Assess the morphology of the erythrocytes.
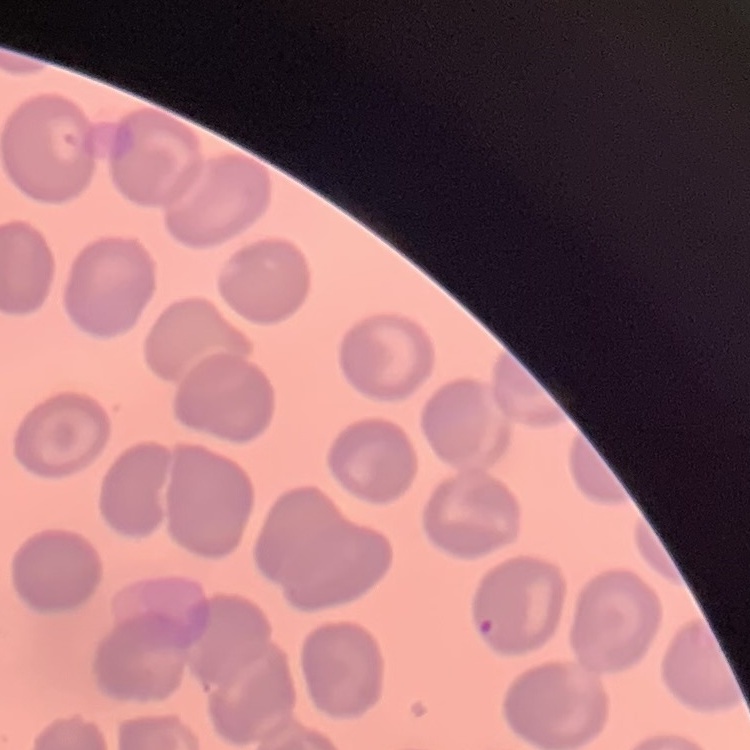
No rouleaux formation.

Summary:
  - Preparation: thin peripheral smear
  - Image type: one tile cut from a larger photomicrograph
  - Stain: Field's or Giemsa